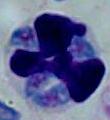 Micrograph. Captured at 1000x magnification. A white blood cell is seen.